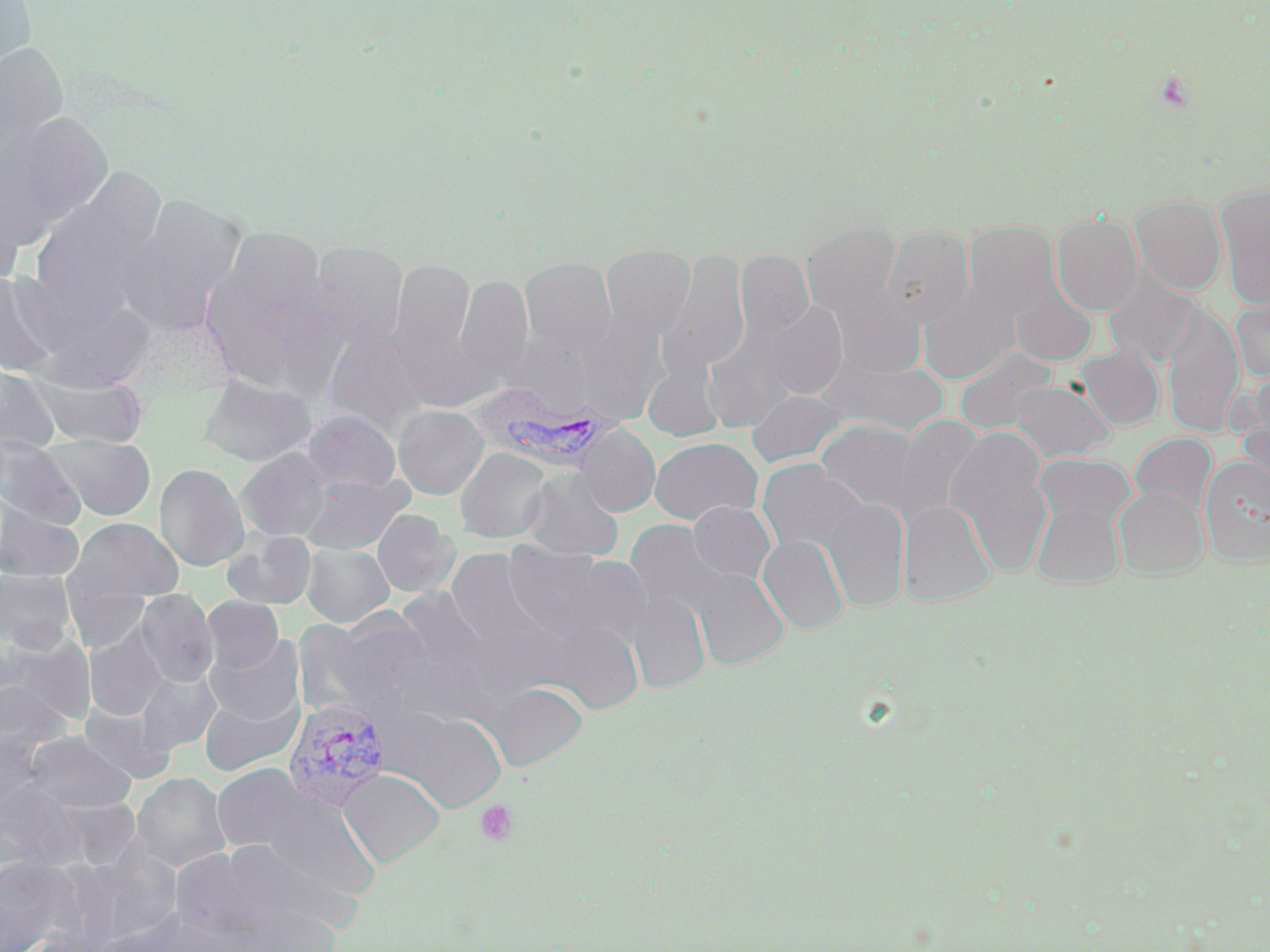
Approximate bounding boxes as named x1/y1/x2/y2 corners in pixels. Uninfected red blood cell locations: (x1=0, y1=0, x2=37, y2=81), (x1=0, y1=42, x2=69, y2=161), (x1=0, y1=112, x2=113, y2=245), (x1=0, y1=179, x2=27, y2=289), (x1=1215, y1=186, x2=1270, y2=309), (x1=28, y1=189, x2=162, y2=321), (x1=118, y1=195, x2=246, y2=335), (x1=1131, y1=195, x2=1227, y2=295), (x1=1051, y1=213, x2=1143, y2=315), (x1=964, y1=221, x2=1059, y2=316), (x1=802, y1=223, x2=901, y2=316), (x1=881, y1=225, x2=973, y2=328), (x1=199, y1=228, x2=337, y2=388), (x1=306, y1=240, x2=409, y2=349), (x1=601, y1=244, x2=695, y2=337), (x1=735, y1=249, x2=814, y2=341), (x1=663, y1=250, x2=750, y2=375), (x1=389, y1=258, x2=476, y2=370), (x1=519, y1=259, x2=616, y2=356), (x1=1103, y1=271, x2=1199, y2=367), (x1=0, y1=272, x2=66, y2=380), (x1=450, y1=274, x2=533, y2=394), (x1=1011, y1=286, x2=1097, y2=366), (x1=830, y1=287, x2=927, y2=379), (x1=919, y1=288, x2=1019, y2=385), (x1=1230, y1=294, x2=1270, y2=384), (x1=760, y1=302, x2=848, y2=400), (x1=1160, y1=304, x2=1244, y2=436), (x1=561, y1=316, x2=667, y2=425), (x1=320, y1=321, x2=437, y2=430), (x1=1076, y1=343, x2=1164, y2=430), (x1=956, y1=352, x2=1053, y2=434), (x1=643, y1=356, x2=725, y2=442), (x1=824, y1=358, x2=950, y2=437), (x1=0, y1=365, x2=59, y2=456), (x1=33, y1=371, x2=151, y2=449), (x1=198, y1=373, x2=317, y2=467), (x1=1010, y1=380, x2=1113, y2=462), (x1=746, y1=389, x2=845, y2=467), (x1=393, y1=404, x2=489, y2=500), (x1=303, y1=409, x2=400, y2=494), (x1=1237, y1=412, x2=1270, y2=515), (x1=895, y1=415, x2=984, y2=522), (x1=816, y1=419, x2=926, y2=516), (x1=575, y1=424, x2=659, y2=516), (x1=946, y1=427, x2=1053, y2=577), (x1=1129, y1=433, x2=1217, y2=516), (x1=45, y1=434, x2=156, y2=521), (x1=649, y1=437, x2=762, y2=526), (x1=0, y1=438, x2=85, y2=530), (x1=455, y1=447, x2=553, y2=544), (x1=236, y1=448, x2=335, y2=542), (x1=1033, y1=453, x2=1136, y2=531), (x1=1199, y1=457, x2=1269, y2=565), (x1=756, y1=458, x2=868, y2=558), (x1=154, y1=463, x2=250, y2=571), (x1=520, y1=468, x2=624, y2=561), (x1=298, y1=474, x2=411, y2=555), (x1=1114, y1=487, x2=1209, y2=579), (x1=824, y1=498, x2=910, y2=612), (x1=898, y1=500, x2=995, y2=606), (x1=687, y1=501, x2=775, y2=586), (x1=1031, y1=502, x2=1124, y2=588), (x1=0, y1=504, x2=84, y2=582), (x1=372, y1=509, x2=460, y2=598), (x1=65, y1=518, x2=183, y2=609), (x1=221, y1=530, x2=316, y2=611), (x1=757, y1=534, x2=849, y2=634), (x1=301, y1=543, x2=393, y2=627), (x1=502, y1=543, x2=620, y2=642), (x1=690, y1=567, x2=789, y2=670), (x1=0, y1=570, x2=76, y2=656), (x1=626, y1=584, x2=711, y2=693), (x1=134, y1=590, x2=217, y2=687), (x1=202, y1=597, x2=283, y2=676), (x1=323, y1=606, x2=436, y2=712), (x1=84, y1=630, x2=167, y2=720), (x1=1, y1=633, x2=94, y2=733), (x1=206, y1=634, x2=304, y2=726), (x1=135, y1=668, x2=221, y2=755), (x1=484, y1=681, x2=587, y2=773), (x1=199, y1=686, x2=303, y2=776), (x1=78, y1=702, x2=173, y2=784), (x1=381, y1=706, x2=507, y2=812), (x1=21, y1=731, x2=136, y2=815), (x1=211, y1=763, x2=316, y2=855), (x1=338, y1=768, x2=446, y2=867), (x1=132, y1=772, x2=228, y2=871), (x1=244, y1=787, x2=383, y2=905), (x1=200, y1=839, x2=352, y2=943), (x1=42, y1=846, x2=176, y2=951), (x1=0, y1=855, x2=74, y2=952). Platelet locations: (x1=1153, y1=70, x2=1195, y2=112), (x1=475, y1=800, x2=519, y2=845). Plasmodium vivax-infected red blood cell locations: (x1=470, y1=387, x2=622, y2=472), (x1=282, y1=697, x2=391, y2=811). Slide-level diagnosis: Plasmodium vivax. Captured at 1000x magnification. Thin blood film. Light microscopy. Single field of view. Image is 1270×952 pixels. May-Grünwald-Giemsa-stained preparation.